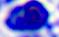
Captured at 400x magnification. Photomicrograph. A leukocyte is seen.